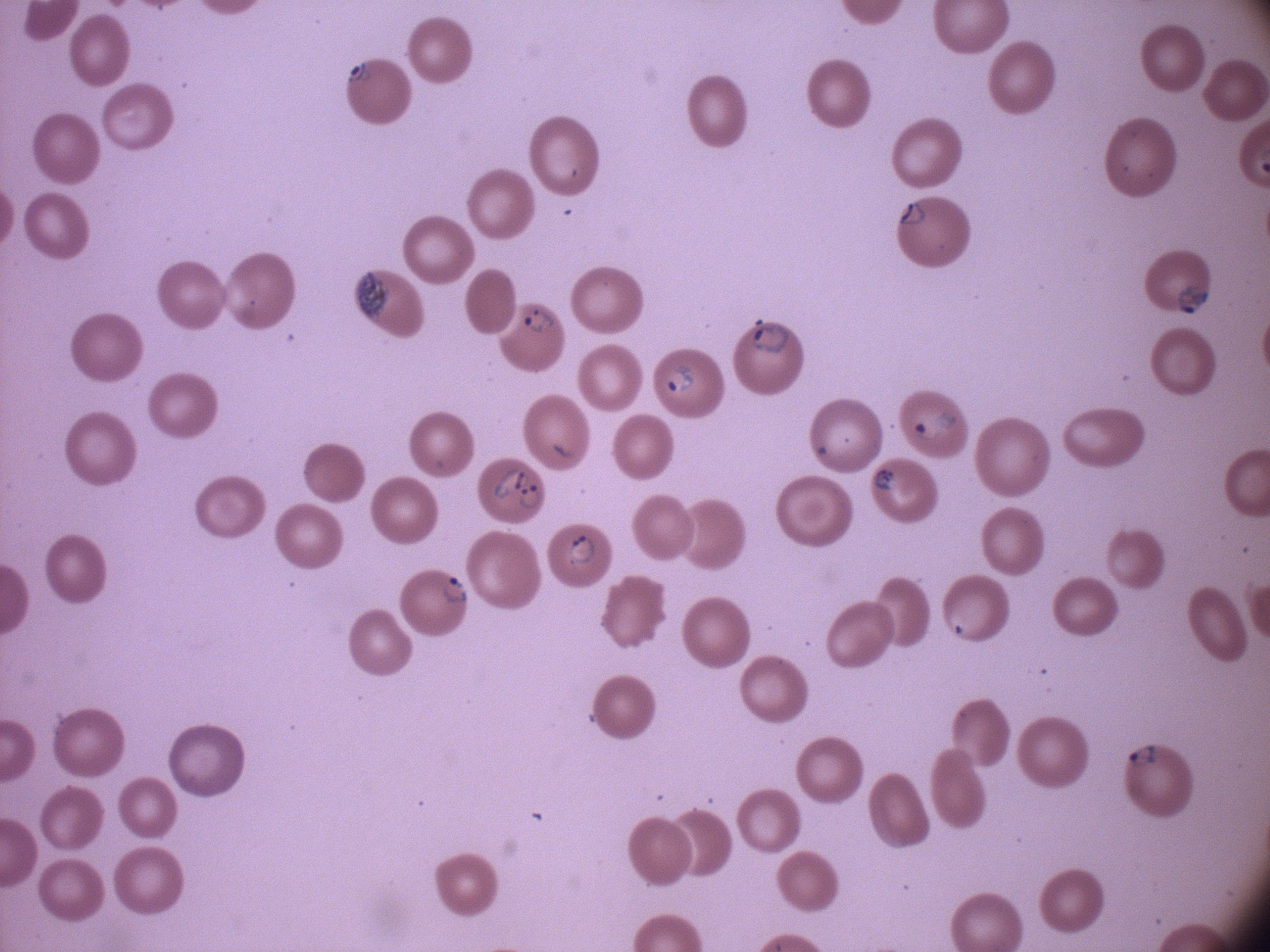
Approximate bounding boxes as (x1,y1)-(x2,y2) corner pairs in pixels, from the source annotation, which is not necessarily exhaustive.
Summary:
  - Ring form locations: (341,58)-(374,88), (898,199)-(929,228), (1172,277)-(1217,317), (521,303)-(561,337), (748,312)-(796,357), (666,361)-(696,399), (905,407)-(963,446), (491,463)-(531,503), (871,467)-(905,494), (514,478)-(548,513), (567,532)-(598,568), (436,571)-(475,608), (1124,740)-(1162,770)
  - Preparation: thin blood smear
  - Field of view: single
  - Microscope: Leica DM2000 with built-in camera
  - Stain: Giemsa
  - Species: Plasmodium falciparum
  - Image size: 1270×952 pixels
  - Magnification: 100x